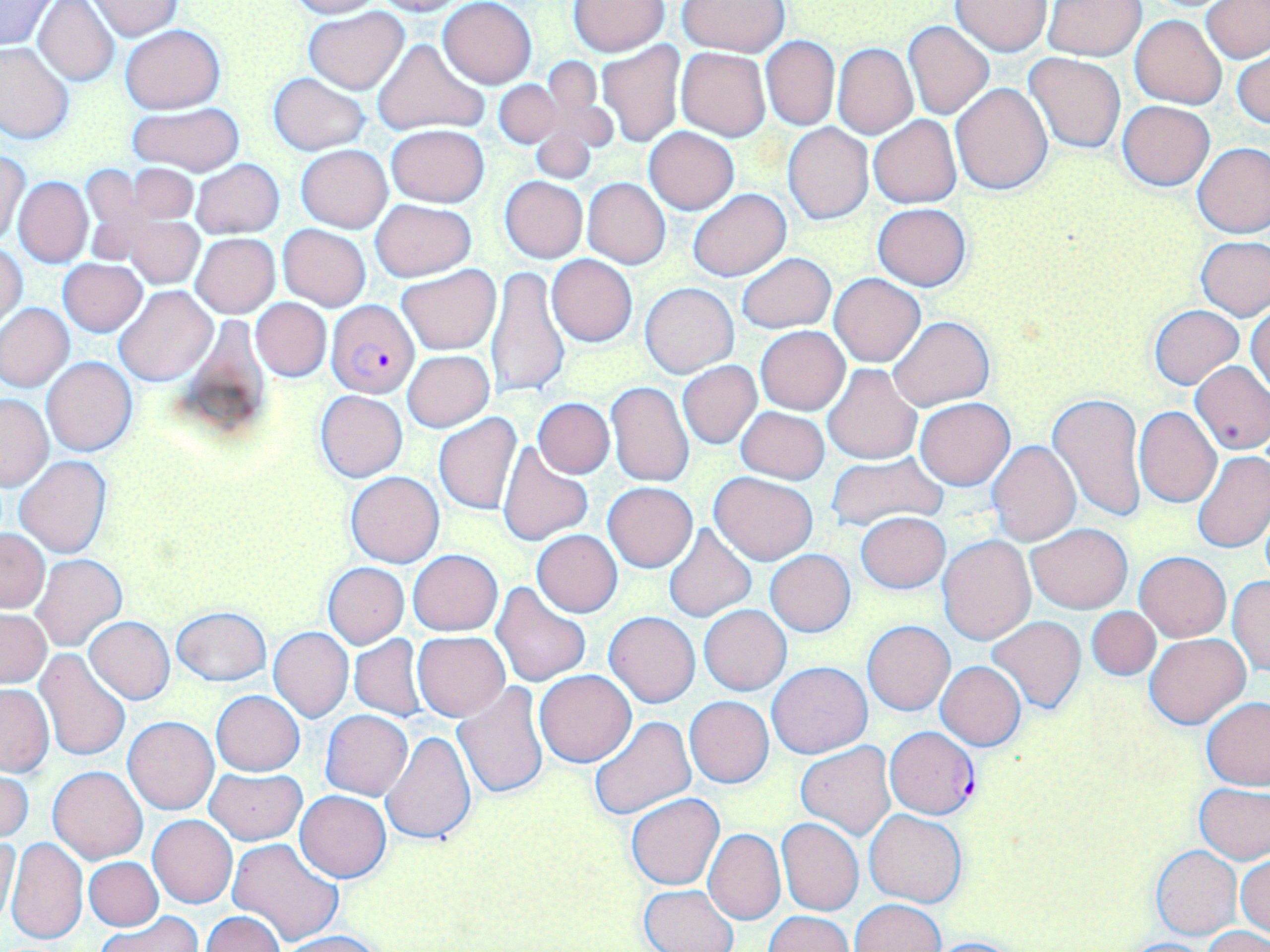
slide-level diagnosis = Plasmodium falciparum
preparation = thin blood film
field of view = single
image size = 1270×952 pixels
Plasmodium falciparum-infected red blood cell locations = approximate bounding boxes as (x1,y1)-(x2,y2) corner pairs in pixels: (325,299)-(420,397), (885,725)-(980,819)
magnification = 1000x
uninfected red blood cell locations = approximate bounding boxes as (x1,y1)-(x2,y2) corner pairs in pixels: (289,0)-(383,18), (372,0)-(466,15), (438,0)-(536,88), (0,1)-(55,50), (34,1)-(120,86), (568,1)-(669,56), (678,1)-(788,55), (951,1)-(1052,55), (1044,1)-(1146,60), (88,2)-(184,38), (1202,2)-(1269,63), (303,7)-(410,94), (1131,15)-(1226,108), (902,20)-(996,120), (120,23)-(224,113), (762,37)-(839,130), (371,39)-(489,136), (0,41)-(74,145), (598,41)-(685,147), (833,44)-(918,139), (676,48)-(770,140), (1233,50)-(1269,132), (1024,52)-(1126,154), (537,59)-(615,158), (268,73)-(371,155), (494,80)-(561,149), (951,83)-(1054,194), (1119,101)-(1213,191), (127,102)-(244,176), (528,111)-(602,184), (868,115)-(962,209), (784,123)-(873,225), (386,124)-(490,208), (645,127)-(738,214), (1193,142)-(1270,238), (296,144)-(393,232), (289,147)-(381,312), (1,150)-(29,246), (190,159)-(285,238), (124,163)-(199,226), (80,165)-(146,263), (13,176)-(93,267), (500,176)-(588,262), (582,178)-(671,269), (687,189)-(791,280), (370,199)-(475,281), (873,204)-(971,291), (123,216)-(203,288), (278,224)-(370,311), (191,233)-(280,318), (1196,235)-(1269,320), (1,244)-(27,327), (736,252)-(836,334), (546,254)-(637,346), (58,258)-(147,336), (397,264)-(501,355), (486,266)-(570,400), (830,273)-(925,367), (640,282)-(739,377), (115,286)-(216,387), (1248,298)-(1270,395), (251,299)-(331,381), (0,303)-(74,391), (1149,305)-(1244,389), (889,315)-(994,410), (756,326)-(850,415), (403,351)-(493,432), (42,356)-(138,457), (677,361)-(762,449), (1189,361)-(1270,455), (823,363)-(921,464), (606,382)-(695,487), (314,390)-(407,482), (1047,392)-(1146,523), (0,393)-(52,490), (532,398)-(615,478), (915,399)-(1015,489), (736,406)-(829,483), (1134,406)-(1222,507), (434,413)-(522,515), (988,440)-(1080,546), (498,443)-(594,545), (1193,450)-(1270,554), (827,451)-(948,531), (13,455)-(112,558), (345,471)-(444,567), (710,472)-(818,565), (603,482)-(698,572), (855,512)-(951,593), (1026,523)-(1131,614), (660,524)-(758,623), (0,528)-(49,612), (531,530)-(622,618), (938,535)-(1035,643), (765,549)-(856,636), (409,550)-(502,635), (1136,551)-(1230,641), (31,554)-(127,651), (322,562)-(409,648), (1228,575)-(1270,677), (491,582)-(590,686), (699,605)-(792,695), (1087,606)-(1160,680), (170,607)-(272,686), (0,609)-(52,687), (604,612)-(701,708), (988,616)-(1086,713), (85,617)-(175,705), (863,621)-(954,715), (268,627)-(353,722), (413,632)-(510,721), (1145,633)-(1250,728), (350,635)-(427,720), (34,648)-(133,762), (767,661)-(873,759), (936,661)-(1026,750), (534,669)-(635,766), (454,682)-(551,799), (0,684)-(53,775), (211,690)-(304,776), (685,696)-(774,787), (1202,696)-(1270,790), (320,710)-(413,800), (122,715)-(219,814), (588,715)-(696,821), (381,730)-(477,846), (797,742)-(895,839), (48,766)-(148,863), (206,767)-(306,844), (0,768)-(34,843), (1195,783)-(1269,863), (296,790)-(390,882), (626,793)-(723,889), (865,809)-(967,907), (148,814)-(237,908), (777,818)-(864,916), (702,828)-(784,924), (0,834)-(21,929), (6,837)-(88,946), (228,837)-(345,947), (1151,845)-(1241,939), (1236,853)-(1269,940), (85,857)-(163,930), (640,885)-(737,952), (851,899)-(943,952), (100,911)-(201,952), (202,912)-(285,952), (765,912)-(852,952), (1203,927)-(1270,952), (276,931)-(386,952), (920,936)-(1032,951), (1118,937)-(1216,952)
stain = May-Grünwald-Giemsa
modality = optical microscopy